Name the parasite shown.
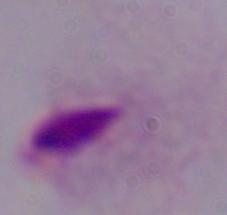
A trichomonad.

Photomicrograph. 1000x magnification.